Classify this cell by malaria status.
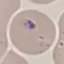

Uninfected.

Photographed with a smartphone camera at the microscope eyepiece. Cell patch, automatically extracted from a larger field of view and resized to 64 × 64 pixels. Giemsa-stained preparation. Thin blood smear.